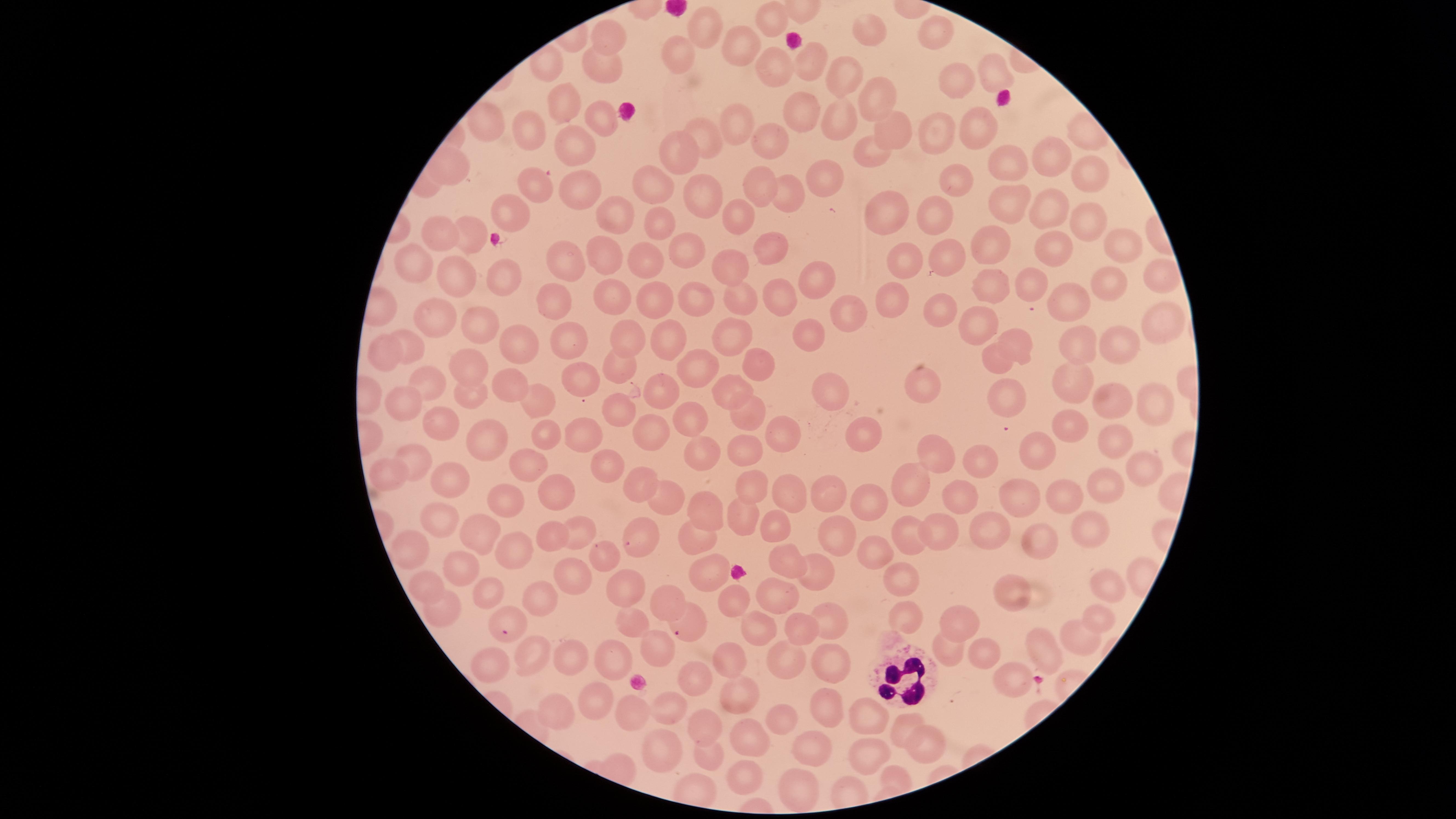
parasitized red blood cells = approximate marker points as [x, y] in pixels: [686, 623], [506, 625]
field of view = single
preparation = thin blood smear
capture = smartphone photograph through the microscope eyepiece
species = Plasmodium falciparum
uninfected red blood cells = approximate marker points as [x, y] in pixels: [770, 15], [704, 27], [871, 27], [939, 27], [608, 33], [742, 44], [674, 56], [811, 62], [604, 63], [770, 67], [999, 71], [846, 72], [956, 81], [878, 96], [564, 98], [802, 112], [595, 116], [841, 118], [730, 120], [975, 124], [941, 126], [528, 128], [887, 132], [710, 136], [770, 138], [683, 144], [573, 145], [872, 157], [1048, 159], [1011, 161], [1080, 170], [828, 173], [959, 179], [656, 181], [758, 183], [535, 185], [573, 190], [700, 191], [789, 198], [1010, 203], [512, 209], [884, 210], [618, 212], [944, 215], [1051, 215], [739, 218], [1087, 219], [656, 222], [445, 230], [468, 232], [998, 241], [1118, 241], [1047, 245], [768, 246], [677, 252], [604, 254], [957, 254], [901, 257], [641, 260], [414, 263], [559, 263], [729, 265], [504, 273], [455, 276], [1158, 276], [1106, 282], [817, 286], [989, 286], [1032, 286], [775, 293], [613, 295], [554, 296], [894, 296], [740, 297], [701, 298], [662, 301], [1078, 301], [853, 315], [941, 315], [436, 316], [486, 322], [734, 324], [1160, 324], [975, 325], [809, 332], [516, 335], [630, 335], [567, 338], [673, 339], [1019, 340], [1080, 343], [410, 346], [1117, 346], [384, 349], [621, 360], [996, 360], [700, 362], [755, 362], [467, 366], [1081, 377], [433, 378], [570, 378], [926, 380], [509, 384], [731, 388], [668, 391], [834, 391], [1008, 394], [471, 395], [1150, 398], [404, 399], [1114, 399], [536, 400], [749, 407], [626, 408], [697, 414], [443, 423], [1068, 427], [782, 431], [586, 432], [548, 433], [654, 434], [489, 437], [861, 437], [1039, 442], [1121, 445], [706, 447], [751, 449], [935, 450], [607, 461], [418, 462], [981, 462], [529, 465], [386, 473], [1136, 474], [448, 478], [753, 481], [1106, 481], [635, 482], [908, 482], [1059, 488], [834, 489], [562, 490], [661, 493], [784, 494], [1028, 494], [963, 496], [867, 498], [507, 503], [706, 505], [744, 517], [439, 523], [643, 525], [777, 527], [993, 527], [475, 531], [938, 531], [912, 533], [1096, 533], [548, 534], [1028, 535], [584, 536], [699, 543], [834, 544], [410, 546], [876, 549], [509, 551], [785, 556], [601, 557], [462, 564], [710, 567], [816, 568], [900, 575], [427, 583], [575, 584], [1103, 588], [491, 589], [633, 592], [1018, 592], [543, 598], [778, 598], [663, 600], [733, 607], [441, 611], [905, 612], [1102, 616], [823, 619], [635, 626], [960, 627], [761, 632], [799, 632], [1077, 636], [661, 651], [948, 651], [734, 652], [1045, 652], [987, 655], [828, 657], [565, 658], [616, 659], [530, 660], [786, 664], [498, 669], [692, 677], [1007, 682], [737, 693], [602, 696], [823, 699], [673, 706], [629, 710], [558, 711], [785, 718], [873, 720], [903, 723], [704, 724], [750, 735], [812, 741], [925, 745], [664, 751], [715, 758], [872, 759], [744, 778], [802, 785]
presence = malaria parasites identified
stain = Giemsa
visible region = circular
image size = 1456×819 pixels
white blood cells = approximate marker points as [x, y] in pixels: [899, 675]